Name the blood parasite species.
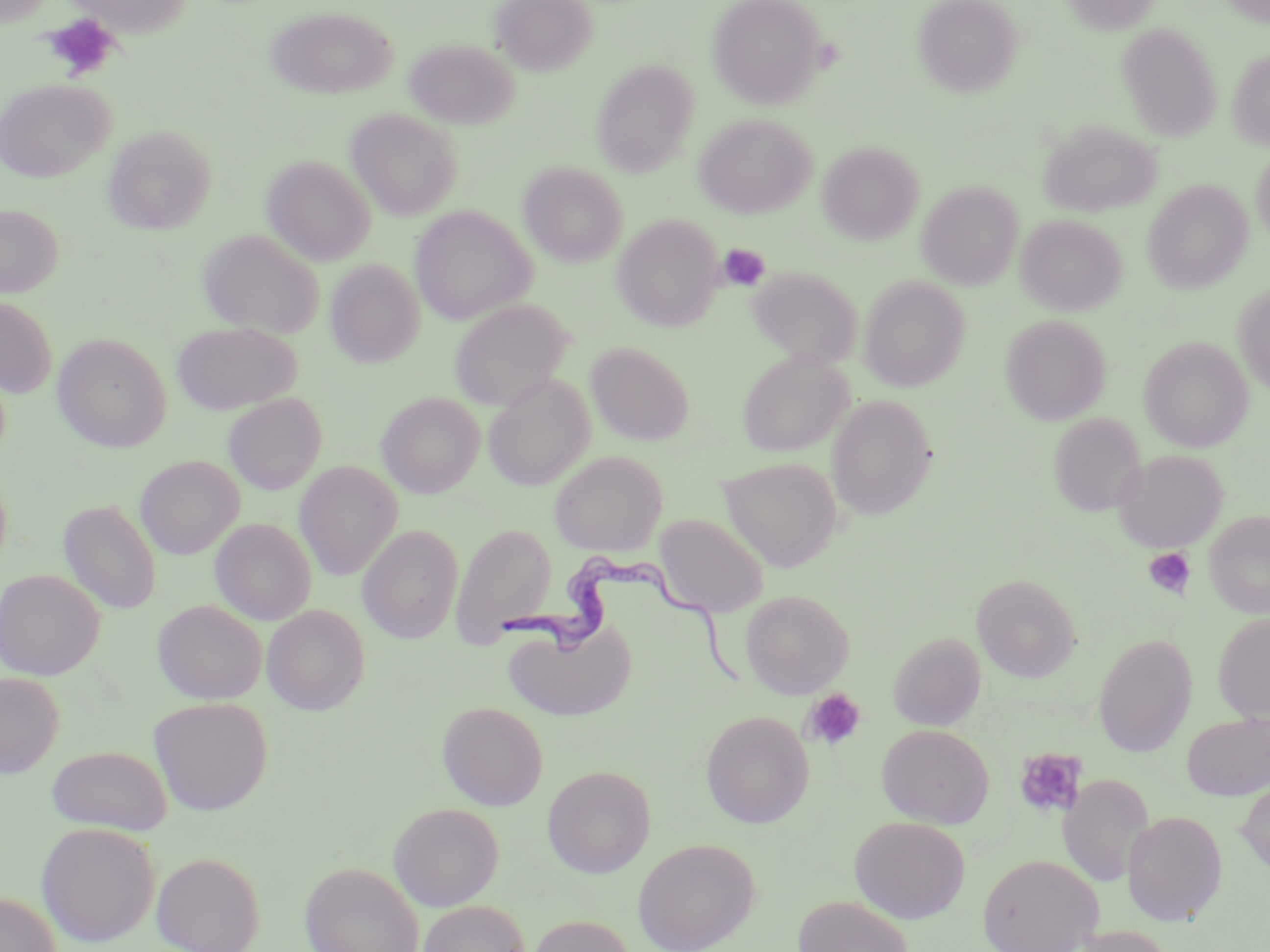

Trypanosoma brucei.

Approximate bounding boxes as (x1, y1, x2, y2) in pixels. Uninfected red blood cell locations: (69, 0, 194, 35), (492, 0, 597, 75), (708, 0, 826, 109), (912, 0, 1023, 97), (1061, 0, 1163, 35), (265, 7, 397, 98), (1117, 23, 1222, 140), (405, 39, 518, 129), (1227, 49, 1270, 149), (591, 60, 700, 176), (0, 78, 115, 182), (347, 108, 463, 220), (694, 113, 816, 218), (1039, 120, 1161, 218), (103, 125, 216, 234), (818, 141, 924, 244), (1250, 147, 1270, 243), (262, 156, 375, 265), (519, 162, 628, 267), (1143, 180, 1253, 292), (917, 181, 1023, 289), (0, 205, 62, 297), (410, 206, 536, 325), (1015, 213, 1127, 316), (613, 215, 722, 332), (198, 229, 324, 339), (326, 259, 424, 367), (746, 265, 865, 369), (858, 276, 970, 391), (1234, 283, 1270, 395), (0, 297, 57, 398), (448, 299, 572, 411), (1000, 314, 1111, 424), (172, 321, 302, 414), (53, 333, 171, 452), (1139, 336, 1253, 452), (586, 341, 695, 445), (736, 351, 853, 457), (484, 374, 595, 490), (377, 392, 485, 497), (223, 393, 327, 494), (827, 395, 937, 520), (1047, 413, 1146, 518), (1113, 449, 1227, 551), (549, 450, 668, 556), (135, 455, 243, 558), (718, 456, 843, 571), (295, 461, 402, 580), (58, 499, 161, 615), (1205, 510, 1270, 617), (655, 514, 769, 618), (211, 519, 316, 625), (449, 522, 557, 644), (358, 525, 464, 643), (0, 568, 105, 680), (971, 573, 1081, 682), (740, 589, 854, 698), (153, 599, 266, 704), (262, 605, 370, 715), (1213, 612, 1270, 723), (503, 616, 636, 721), (888, 631, 986, 731), (1093, 634, 1197, 756), (0, 671, 64, 778), (149, 697, 273, 815), (437, 701, 548, 810), (701, 711, 813, 828), (1182, 711, 1270, 800), (877, 724, 994, 828), (48, 745, 172, 835), (542, 765, 656, 877), (1059, 774, 1153, 886), (1236, 776, 1270, 876), (390, 803, 503, 910), (1122, 811, 1227, 925), (850, 816, 970, 923), (36, 822, 160, 946), (633, 838, 760, 951), (152, 851, 265, 952), (977, 853, 1103, 952), (300, 861, 423, 952), (0, 892, 61, 952), (794, 895, 914, 951), (418, 901, 531, 952), (526, 915, 635, 952), (1067, 925, 1175, 952). Trypanosoma brucei locations: (495, 553, 761, 683). Platelet locations: (43, 14, 120, 81), (716, 243, 771, 292), (1143, 547, 1196, 598), (803, 689, 865, 750), (1015, 748, 1087, 818). One field of a larger specimen. May-Grünwald-Giemsa-stained preparation. Thin blood smear. Light microscopy. Image is 1270×952 pixels. 1000x magnification.